Report the malaria status of this cell.
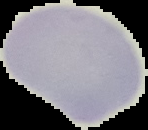

It is uninfected.

Image is 148×130 pixels. From a thin blood smear. Segmented cell region on a black background.